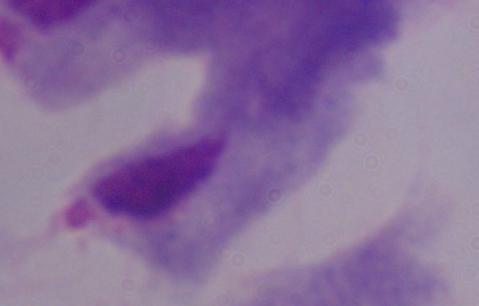
{
  "modality": "micrograph",
  "magnification": "1000x",
  "identification": "trichomonad"
}